Give the preparation type.
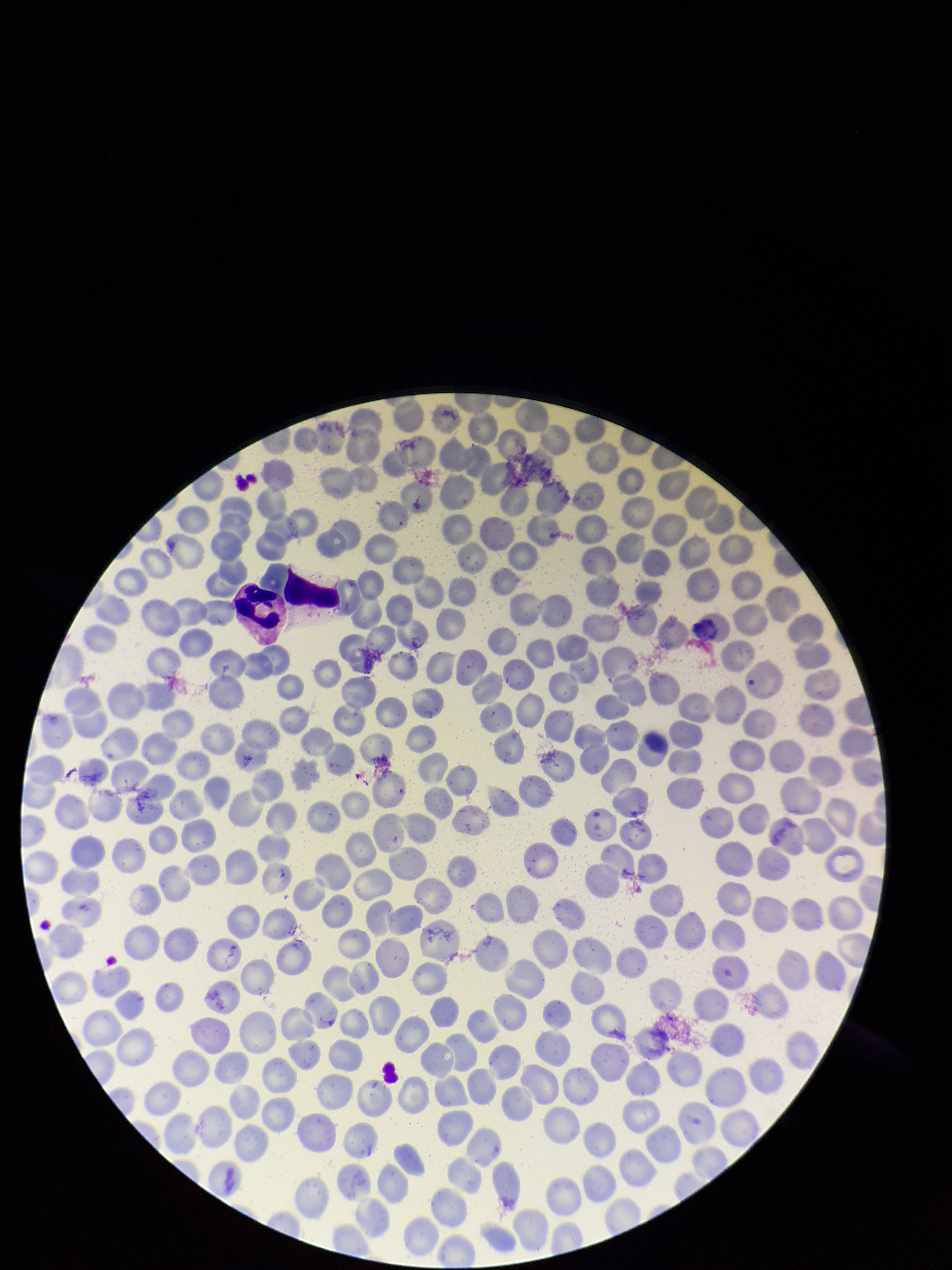
It is a thin blood smear.

{
  "stain": "Giemsa",
  "red_blood_cell_count": 234,
  "capture": "smartphone photograph through the microscope eyepiece",
  "parasitized_red_blood_cell_count": 0,
  "image_size": "952×1270 pixels",
  "parasitized_red_blood_cells": "none seen",
  "field_of_view": "single",
  "patient_malaria_status": "negative"
}